Identify the cell.
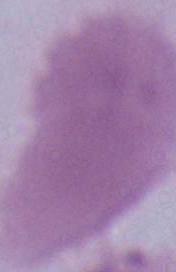
An erythrocyte.

magnification = 1000x
modality = micrograph